Assess this cell for malaria.
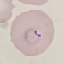
It is parasitized.

Summary:
  - Stain: Giemsa
  - Capture: smartphone through the microscope eyepiece
  - Image type: cell patch, automatically extracted from a larger field of view and resized to 64 × 64 pixels
  - Preparation: thin blood smear